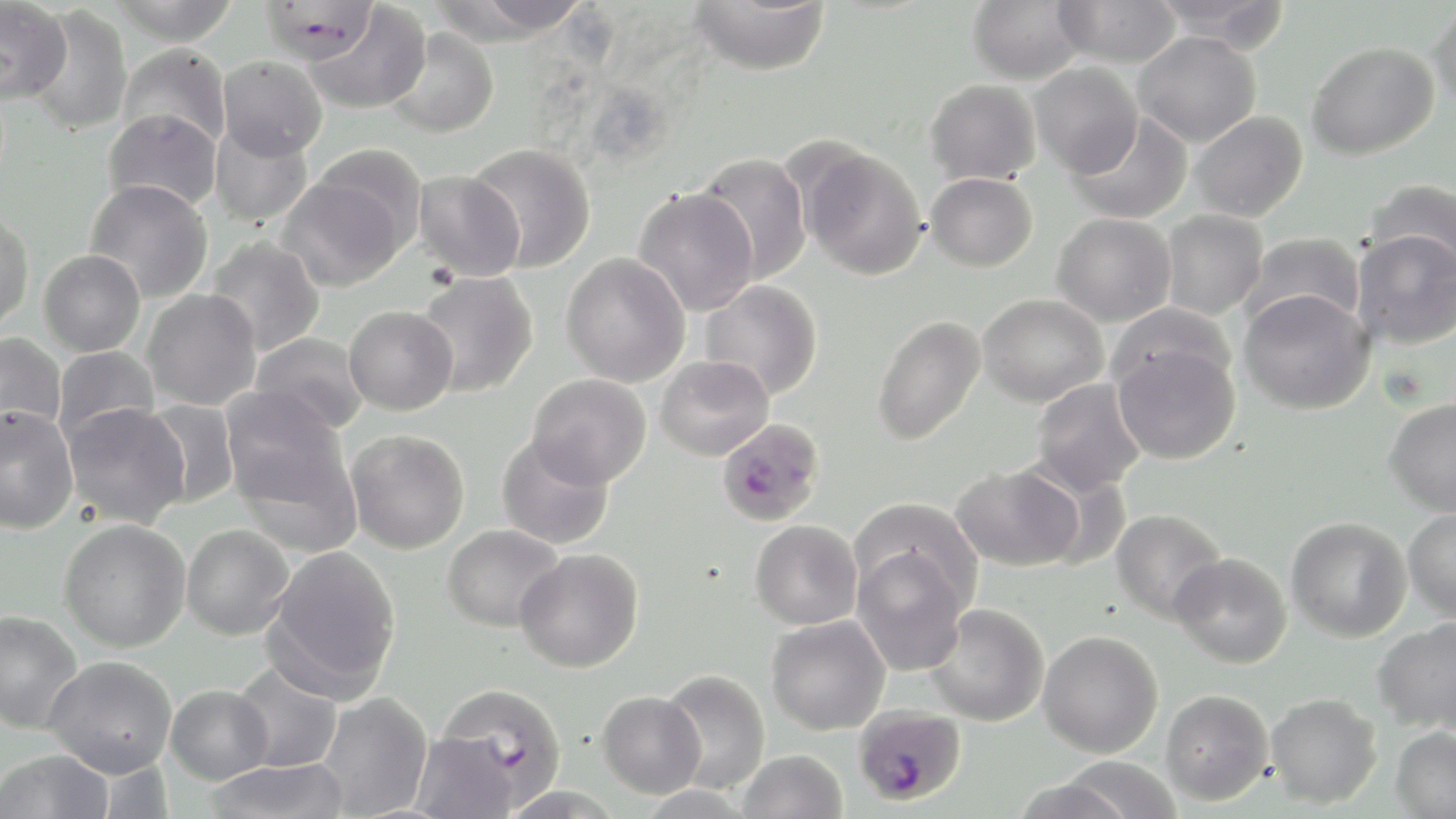

Summary:
  - Coordinate format: approximate bounding boxes as (x1, y1, x2, y2) in pixels
  - Uninfected red blood cell locations: (0, 0, 73, 105), (112, 0, 240, 45), (259, 0, 380, 64), (435, 0, 597, 40), (686, 0, 832, 75), (967, 0, 1088, 85), (1150, 0, 1293, 47), (1053, 1, 1182, 68), (1428, 1, 1456, 115), (305, 3, 431, 115), (25, 4, 132, 135), (384, 27, 499, 139), (1133, 31, 1261, 146), (1306, 41, 1439, 160), (118, 44, 231, 149), (217, 56, 327, 161), (1029, 62, 1143, 177), (925, 79, 1041, 185), (102, 108, 222, 213), (1067, 111, 1193, 225), (1189, 111, 1308, 222), (209, 121, 313, 226), (467, 143, 596, 272), (310, 144, 428, 252), (799, 145, 927, 281), (694, 152, 812, 285), (413, 170, 526, 281), (926, 172, 1038, 271), (277, 176, 407, 291), (85, 179, 214, 302), (1363, 179, 1456, 277), (634, 188, 759, 316), (0, 210, 34, 335), (1160, 210, 1268, 320), (1052, 213, 1176, 327), (1352, 229, 1456, 349), (1243, 232, 1365, 333), (205, 237, 326, 356), (39, 250, 145, 356), (561, 252, 690, 387), (416, 271, 539, 397), (698, 280, 823, 401), (1238, 288, 1375, 415), (141, 289, 262, 410), (977, 293, 1108, 406), (344, 305, 458, 415), (872, 314, 987, 446), (0, 332, 67, 438), (250, 333, 369, 435), (1112, 339, 1242, 465), (53, 345, 159, 444), (655, 355, 774, 461), (527, 374, 651, 488), (1030, 378, 1146, 496), (220, 388, 353, 519), (1384, 397, 1456, 517), (141, 399, 240, 509), (63, 403, 191, 528), (1, 406, 80, 534), (345, 429, 470, 554), (496, 435, 615, 550), (950, 463, 1083, 571), (849, 498, 982, 614), (1110, 508, 1228, 625), (1403, 508, 1456, 623), (1286, 516, 1411, 642), (58, 519, 191, 652), (750, 519, 862, 630), (442, 523, 565, 632), (182, 524, 294, 640), (264, 545, 401, 698), (852, 545, 971, 675), (515, 548, 643, 673), (1170, 552, 1292, 668), (925, 603, 1049, 726), (0, 609, 84, 733), (766, 615, 891, 735), (1371, 618, 1456, 733), (1038, 630, 1163, 757), (45, 655, 177, 777), (229, 663, 343, 773), (658, 670, 770, 794), (166, 684, 273, 784), (1161, 688, 1273, 805), (596, 690, 706, 798), (316, 692, 433, 818), (1265, 692, 1382, 809), (1390, 727, 1456, 819), (410, 731, 521, 819), (0, 749, 114, 819), (738, 749, 848, 819), (1057, 756, 1184, 818), (201, 758, 350, 819), (1009, 777, 1139, 819)
  - Plasmodium falciparum-infected red blood cell locations: (716, 417, 824, 526), (435, 685, 569, 811), (853, 704, 966, 807)
  - Slide-level diagnosis: Plasmodium falciparum
  - Stain: May-Grünwald-Giemsa
  - Modality: optical microscopy
  - Preparation: thin blood film
  - Field of view: one of a larger specimen
  - Magnification: 1000x
  - Image size: 1456×819 pixels